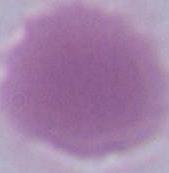

magnification = 1000x
modality = micrograph
identification = red blood cell